Identify the blood parasite species.
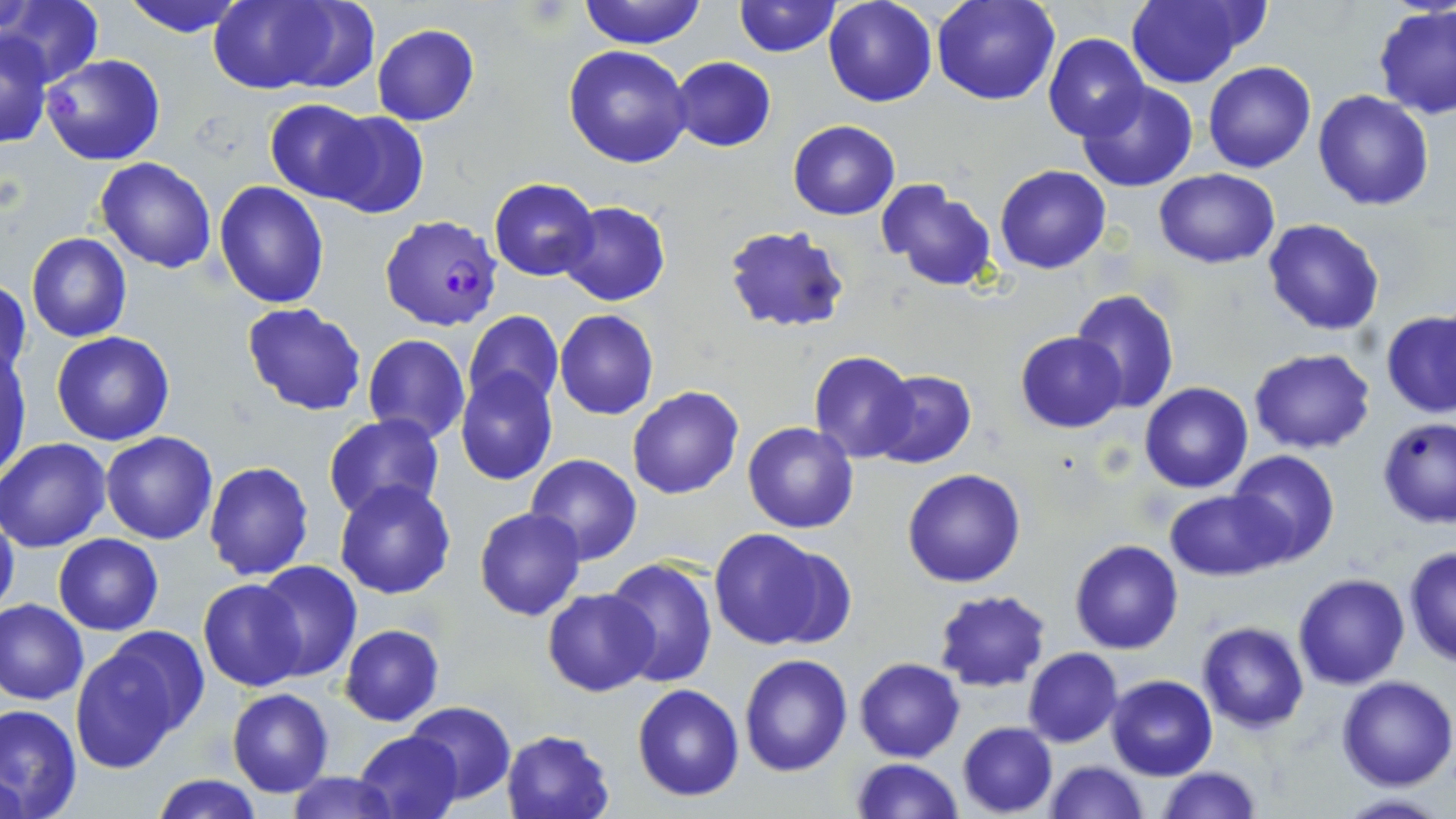

Plasmodium falciparum.

Summary:
  - Coordinate format: approximate bounding boxes as named x1/y1/x2/y2 corners in pixels
  - Plasmodium falciparum-infected red blood cell locations: (x1=378, y1=214, x2=504, y2=332)
  - Uninfected red blood cell locations: (x1=119, y1=0, x2=251, y2=38), (x1=207, y1=0, x2=354, y2=93), (x1=579, y1=0, x2=706, y2=48), (x1=732, y1=0, x2=840, y2=56), (x1=823, y1=0, x2=937, y2=106), (x1=931, y1=0, x2=1059, y2=105), (x1=1123, y1=0, x2=1257, y2=89), (x1=2, y1=2, x2=103, y2=88), (x1=1373, y1=5, x2=1456, y2=119), (x1=371, y1=24, x2=479, y2=126), (x1=1043, y1=32, x2=1150, y2=142), (x1=1, y1=33, x2=52, y2=149), (x1=563, y1=45, x2=692, y2=167), (x1=39, y1=54, x2=166, y2=167), (x1=668, y1=57, x2=776, y2=152), (x1=1203, y1=61, x2=1315, y2=173), (x1=1076, y1=81, x2=1198, y2=192), (x1=1314, y1=91, x2=1434, y2=211), (x1=265, y1=101, x2=376, y2=203), (x1=317, y1=110, x2=429, y2=220), (x1=787, y1=120, x2=899, y2=219), (x1=96, y1=157, x2=217, y2=273), (x1=994, y1=165, x2=1110, y2=274), (x1=1153, y1=168, x2=1280, y2=269), (x1=489, y1=178, x2=598, y2=282), (x1=214, y1=180, x2=330, y2=309), (x1=876, y1=180, x2=999, y2=292), (x1=556, y1=201, x2=671, y2=306), (x1=1261, y1=218, x2=1385, y2=336), (x1=721, y1=225, x2=852, y2=332), (x1=26, y1=233, x2=130, y2=342), (x1=1, y1=278, x2=30, y2=383), (x1=1070, y1=289, x2=1180, y2=414), (x1=242, y1=303, x2=368, y2=417), (x1=554, y1=310, x2=659, y2=420), (x1=463, y1=311, x2=564, y2=413), (x1=1382, y1=311, x2=1456, y2=419), (x1=51, y1=331, x2=175, y2=446), (x1=1016, y1=331, x2=1127, y2=432), (x1=362, y1=333, x2=471, y2=445), (x1=1, y1=346, x2=32, y2=478), (x1=1249, y1=349, x2=1376, y2=454), (x1=809, y1=352, x2=916, y2=463), (x1=456, y1=370, x2=558, y2=486), (x1=868, y1=370, x2=975, y2=469), (x1=1139, y1=382, x2=1252, y2=494), (x1=627, y1=385, x2=743, y2=499), (x1=322, y1=415, x2=446, y2=523), (x1=1376, y1=417, x2=1456, y2=529), (x1=742, y1=420, x2=859, y2=533), (x1=100, y1=430, x2=218, y2=544), (x1=0, y1=437, x2=112, y2=553), (x1=1227, y1=449, x2=1340, y2=566), (x1=525, y1=455, x2=642, y2=565), (x1=203, y1=460, x2=315, y2=581), (x1=902, y1=467, x2=1027, y2=587), (x1=333, y1=479, x2=457, y2=600), (x1=1165, y1=489, x2=1285, y2=580), (x1=474, y1=507, x2=586, y2=621), (x1=0, y1=510, x2=20, y2=623), (x1=707, y1=528, x2=839, y2=650), (x1=54, y1=533, x2=163, y2=635), (x1=1069, y1=539, x2=1183, y2=654), (x1=1403, y1=545, x2=1455, y2=667), (x1=605, y1=556, x2=719, y2=687), (x1=252, y1=562, x2=363, y2=682), (x1=1294, y1=573, x2=1409, y2=689), (x1=198, y1=579, x2=306, y2=691), (x1=542, y1=588, x2=660, y2=696), (x1=932, y1=589, x2=1051, y2=692), (x1=1, y1=599, x2=89, y2=705), (x1=1196, y1=622, x2=1309, y2=734), (x1=340, y1=624, x2=444, y2=725), (x1=71, y1=638, x2=193, y2=772), (x1=1023, y1=647, x2=1122, y2=748), (x1=740, y1=653, x2=852, y2=775), (x1=855, y1=657, x2=964, y2=762), (x1=1106, y1=675, x2=1217, y2=780), (x1=1335, y1=675, x2=1456, y2=790), (x1=632, y1=683, x2=744, y2=801), (x1=228, y1=688, x2=333, y2=797), (x1=405, y1=701, x2=515, y2=802), (x1=0, y1=704, x2=81, y2=818), (x1=957, y1=721, x2=1057, y2=816), (x1=501, y1=729, x2=616, y2=819), (x1=353, y1=730, x2=464, y2=819), (x1=851, y1=758, x2=962, y2=818), (x1=1043, y1=760, x2=1148, y2=819), (x1=1157, y1=767, x2=1263, y2=818), (x1=287, y1=773, x2=403, y2=818), (x1=151, y1=775, x2=264, y2=818), (x1=1332, y1=793, x2=1452, y2=819)
  - Field of view: single
  - Image size: 1456×819 pixels
  - Stain: May-Grünwald-Giemsa
  - Modality: optical microscopy
  - Preparation: thin blood film
  - Magnification: 1000x